State which parasite is depicted.
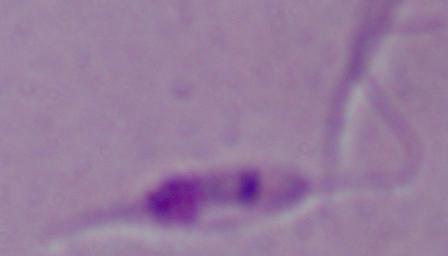

This is Leishmania.

Photomicrograph. 1000x magnification.